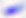

Summary:
  - Modality: photomicrograph
  - Magnification: 400x
  - Identification: Toxoplasma gondii